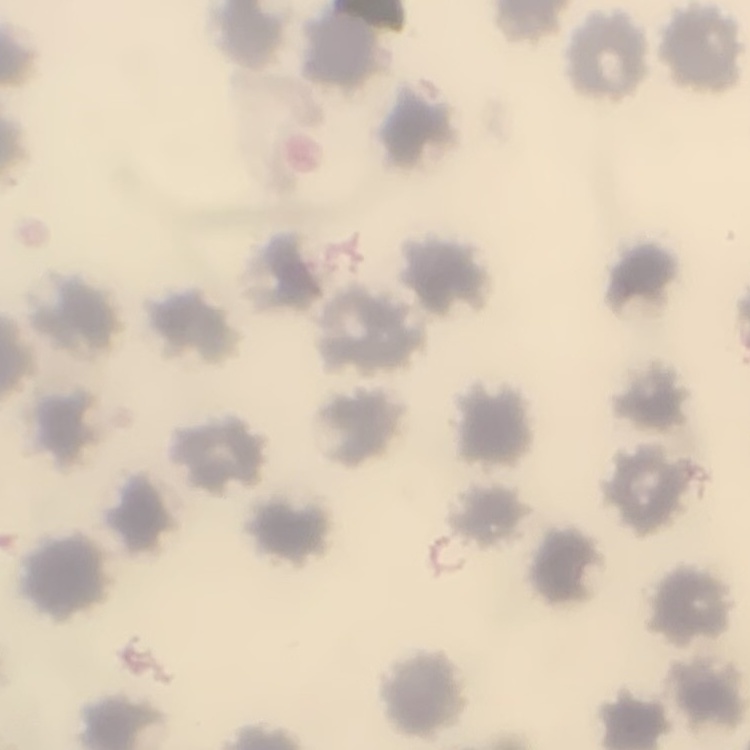

Summary:
  - Erythrocyte morphology: no rouleaux formation
  - Image type: square crop of a larger photomicrograph
  - Stain: Field's or Giemsa
  - Preparation: thin blood smear